Give the extent of all uninfected red blood cells.
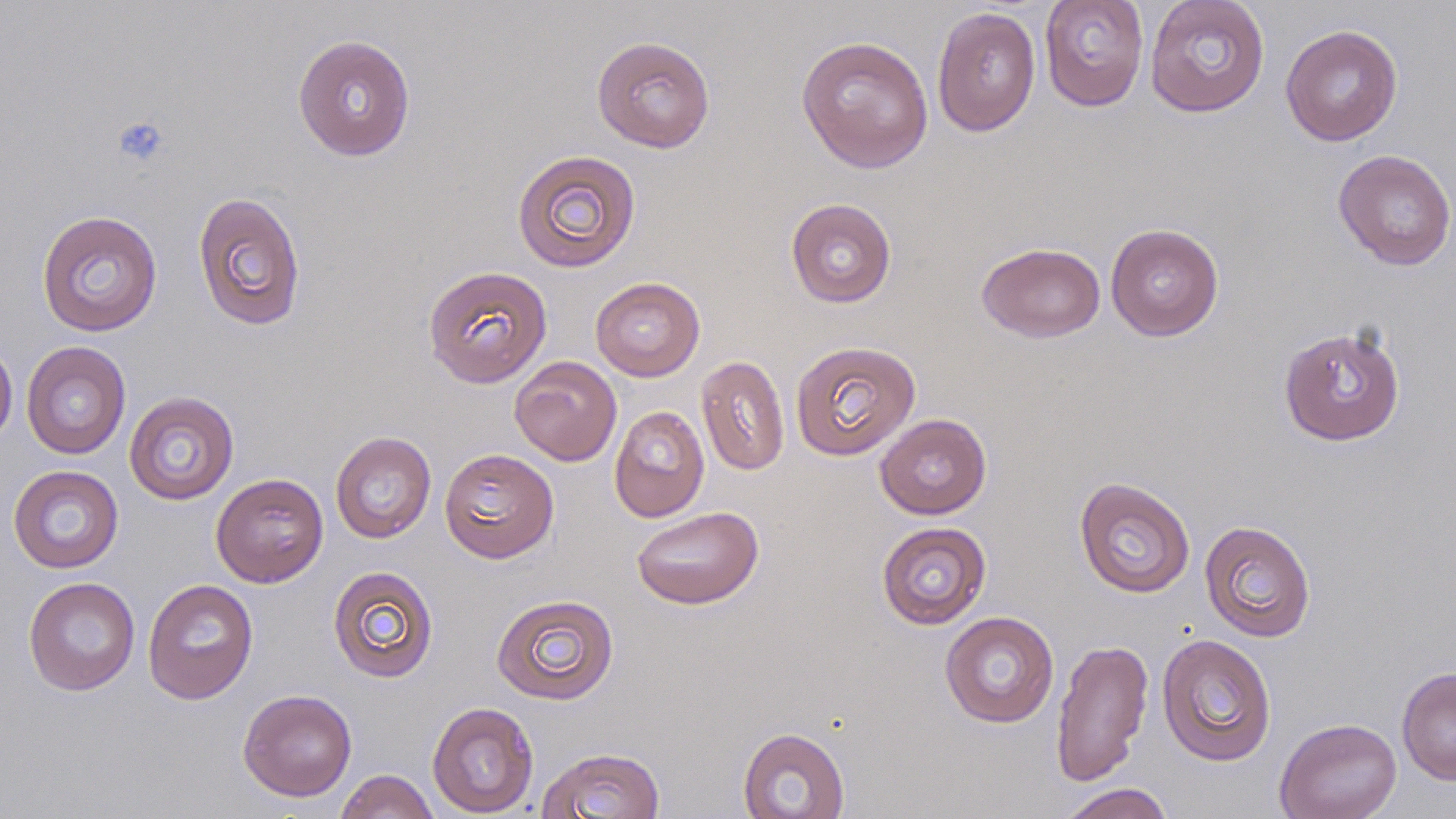
Approximate bounding boxes as [x1, y1, x2, y2] in pixels.
Uninfected red blood cells: [1039, 0, 1149, 112], [1144, 0, 1270, 118], [931, 6, 1041, 137], [1280, 24, 1403, 146], [292, 34, 417, 161], [796, 35, 934, 174], [591, 36, 716, 153], [511, 149, 642, 273], [1333, 149, 1456, 271], [192, 191, 306, 331], [785, 197, 897, 308], [36, 209, 163, 337], [1105, 223, 1224, 341], [977, 242, 1106, 343], [423, 265, 552, 388], [590, 276, 705, 382], [1278, 324, 1406, 446], [0, 338, 18, 446], [790, 340, 921, 461], [21, 341, 131, 460], [696, 355, 790, 476], [509, 356, 622, 466], [124, 391, 240, 505], [608, 405, 709, 522], [875, 413, 992, 519], [330, 431, 437, 544], [439, 447, 559, 563], [8, 465, 124, 573], [211, 472, 329, 587], [1074, 477, 1196, 598], [631, 506, 764, 610], [1199, 519, 1316, 642], [876, 521, 992, 630], [328, 565, 439, 683], [23, 576, 140, 696], [142, 578, 259, 705], [491, 593, 619, 705], [939, 611, 1059, 728], [1156, 633, 1277, 767], [1051, 638, 1153, 787], [1397, 666, 1456, 786], [238, 688, 357, 801], [427, 701, 539, 818], [1273, 717, 1403, 819], [738, 727, 850, 819], [536, 746, 666, 819], [335, 769, 439, 819], [1057, 783, 1175, 819].

Platelet locations: [111, 114, 170, 167]. Slide-level diagnosis: negative for blood parasites. May-Grünwald-Giemsa-stained preparation. One field of a larger specimen. Thin blood smear. Image is 1456×819 pixels. Captured at 1000x magnification. Optical microscopy.